Name the parasite shown.
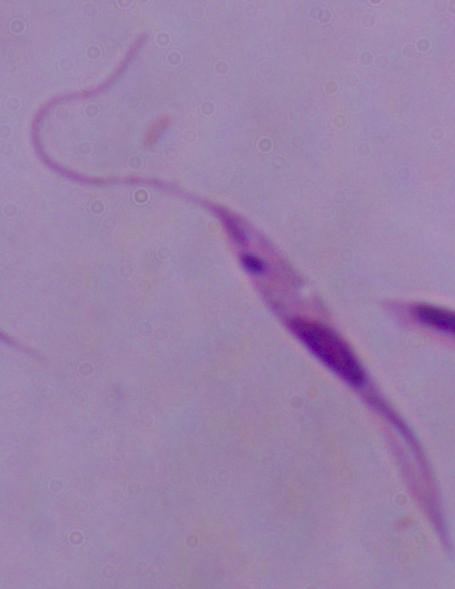
This is Leishmania.

Micrograph. 1000x magnification.